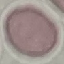

Summary:
  - Malaria status: uninfected
  - Preparation: thin blood film
  - Stain: Giemsa
  - Capture: smartphone camera at the microscope eyepiece
  - Image type: automatically extracted cell patch, resized to 64 × 64 pixels